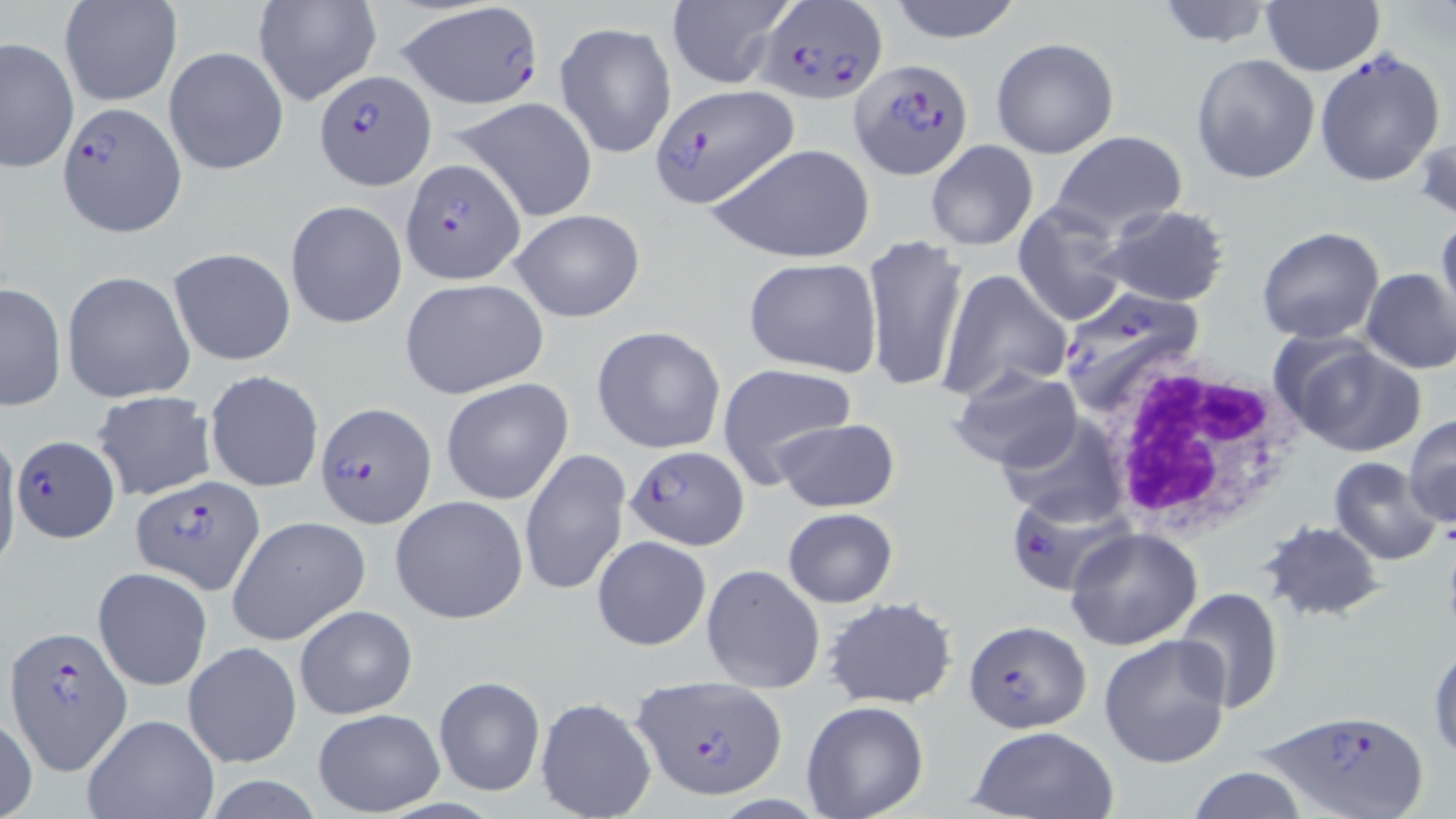
{
  "slide_level_diagnosis": "Plasmodium falciparum",
  "preparation": "thin blood smear",
  "field_of_view": "single",
  "plasmodium_falciparum_infected_red_blood_cell_locations": "approximate bounding boxes as (x1,y1)-(x2,y2) corner pairs in pixels: (394,0)-(547,111), (752,4)-(887,102), (1314,46)-(1447,187), (850,58)-(972,178), (312,68)-(433,189), (653,82)-(799,208), (58,101)-(186,235), (399,158)-(524,283), (1057,285)-(1208,415), (314,402)-(436,528), (13,436)-(121,543), (624,445)-(749,550), (132,475)-(265,595), (1005,492)-(1124,596), (963,619)-(1091,733), (5,626)-(132,773), (632,674)-(788,799), (1262,708)-(1427,819)",
  "white_blood_cell_locations": "approximate bounding boxes as (x1,y1)-(x2,y2) corner pairs in pixels: (1097,358)-(1303,540)",
  "stain": "May-Grünwald-Giemsa",
  "magnification": "1000x",
  "image_size": "1456×819 pixels",
  "uninfected_red_blood_cell_locations": "approximate bounding boxes as (x1,y1)-(x2,y2) corner pairs in pixels: (251,0)-(382,107), (666,0)-(798,90), (884,0)-(1027,44), (1151,0)-(1278,49), (58,1)-(182,108), (1261,1)-(1383,76), (0,15)-(133,158), (554,21)-(677,160), (1,37)-(78,173), (990,37)-(1118,158), (163,46)-(289,175), (1190,53)-(1320,183), (452,96)-(599,221), (1414,124)-(1456,224), (1050,130)-(1186,235), (925,140)-(1038,251), (708,142)-(876,265), (285,200)-(407,328), (1013,202)-(1130,326), (1095,205)-(1233,308), (507,209)-(647,323), (1436,212)-(1456,329), (1257,227)-(1385,344), (863,234)-(969,395), (167,247)-(296,366), (742,257)-(882,375), (1360,268)-(1456,374), (937,269)-(1072,400), (61,270)-(196,403), (1324,275)-(1448,434), (400,277)-(548,397), (1,283)-(67,412), (592,326)-(726,454), (1274,335)-(1428,457), (717,364)-(858,487), (948,366)-(1082,476), (204,370)-(323,492), (441,378)-(574,505), (93,391)-(216,500), (997,412)-(1130,528), (1404,414)-(1456,528), (773,418)-(899,513), (0,434)-(22,578), (519,450)-(630,599), (1328,457)-(1443,566), (390,494)-(529,623), (782,507)-(897,608), (227,515)-(369,646), (1261,522)-(1384,621), (1064,527)-(1204,650), (592,536)-(712,651), (703,564)-(824,693), (93,566)-(212,691), (1175,588)-(1284,714), (825,599)-(956,710), (295,603)-(418,719), (1098,635)-(1231,769), (182,641)-(302,770), (1429,642)-(1456,765), (432,675)-(545,796), (534,696)-(657,819), (802,701)-(930,818), (313,708)-(444,816), (0,711)-(37,819), (82,713)-(220,819), (966,726)-(1118,818), (1183,766)-(1310,819)",
  "modality": "optical microscopy"
}